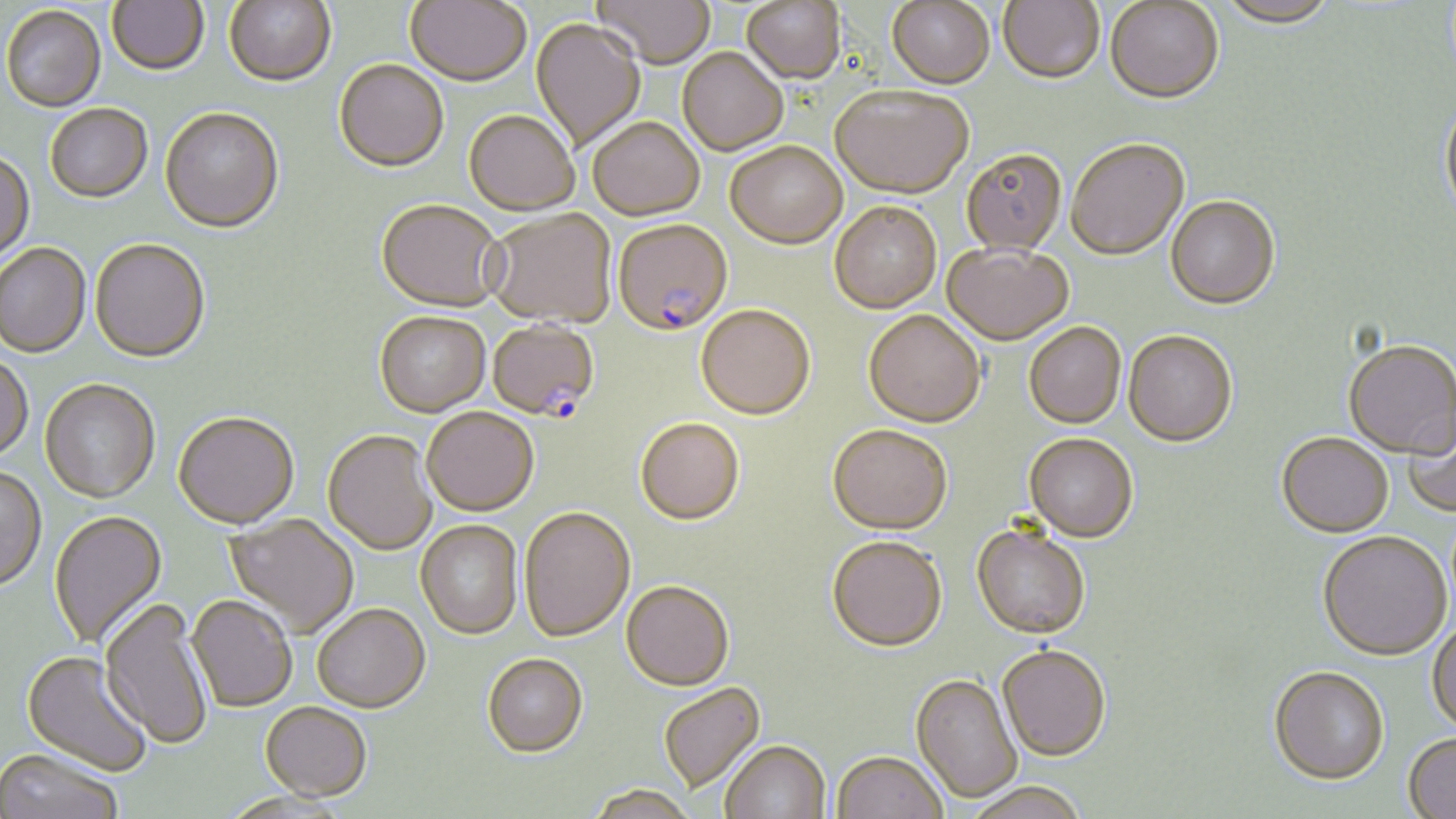

slide-level diagnosis = Plasmodium falciparum
image size = 1456×819 pixels
stain = May-Grünwald-Giemsa
field of view = single
uninfected red blood cell locations = approximate bounding boxes as [x1, y1, x2, y2] in pixels: [107, 0, 210, 77], [405, 0, 531, 89], [592, 0, 715, 72], [742, 0, 847, 88], [224, 1, 336, 89], [887, 1, 995, 91], [998, 1, 1104, 87], [1218, 1, 1336, 30], [1105, 2, 1224, 107], [2, 7, 106, 114], [530, 20, 645, 152], [677, 50, 787, 158], [334, 63, 449, 175], [831, 90, 974, 203], [1440, 100, 1456, 225], [45, 106, 153, 205], [160, 110, 284, 236], [463, 113, 579, 218], [588, 121, 705, 223], [1066, 141, 1190, 263], [725, 145, 847, 253], [0, 153, 35, 268], [961, 153, 1066, 257], [1165, 199, 1280, 312], [375, 202, 505, 315], [830, 204, 941, 316], [486, 211, 616, 331], [90, 241, 210, 365], [0, 244, 92, 359], [942, 247, 1073, 347], [696, 308, 815, 423], [863, 313, 985, 430], [374, 314, 491, 419], [1024, 325, 1126, 431], [1123, 333, 1237, 450], [1343, 343, 1455, 461], [0, 355, 34, 464], [39, 381, 160, 504], [1403, 409, 1456, 519], [421, 410, 539, 519], [173, 414, 299, 531], [636, 420, 745, 528], [827, 427, 952, 539], [323, 432, 437, 557], [1277, 435, 1394, 541], [1023, 436, 1137, 545], [0, 466, 48, 593], [519, 509, 635, 645], [49, 511, 168, 651], [224, 515, 359, 639], [415, 522, 523, 641], [971, 529, 1090, 641], [1317, 534, 1452, 663], [827, 540, 948, 656], [621, 583, 734, 694], [186, 597, 297, 714], [98, 600, 213, 751], [312, 606, 430, 715], [1427, 622, 1456, 737], [997, 648, 1111, 765], [21, 651, 152, 778], [482, 657, 588, 761], [1269, 670, 1390, 789], [910, 676, 1022, 804], [659, 684, 767, 795], [260, 704, 371, 804], [1402, 735, 1456, 819], [721, 743, 831, 819], [0, 750, 123, 819], [832, 754, 947, 819], [959, 785, 1092, 819], [585, 787, 698, 818]
modality = optical microscopy
preparation = thin blood film
Plasmodium falciparum-infected red blood cell locations = approximate bounding boxes as [x1, y1, x2, y2] in pixels: [614, 223, 732, 339], [488, 323, 599, 426]
magnification = 1000x